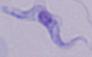
Captured at 1000x magnification. Photomicrograph. A trypanosome is shown.